State which parasite is depicted.
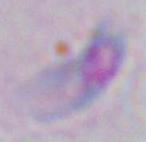

This is Toxoplasma gondii.

Photomicrograph. 1000x magnification.